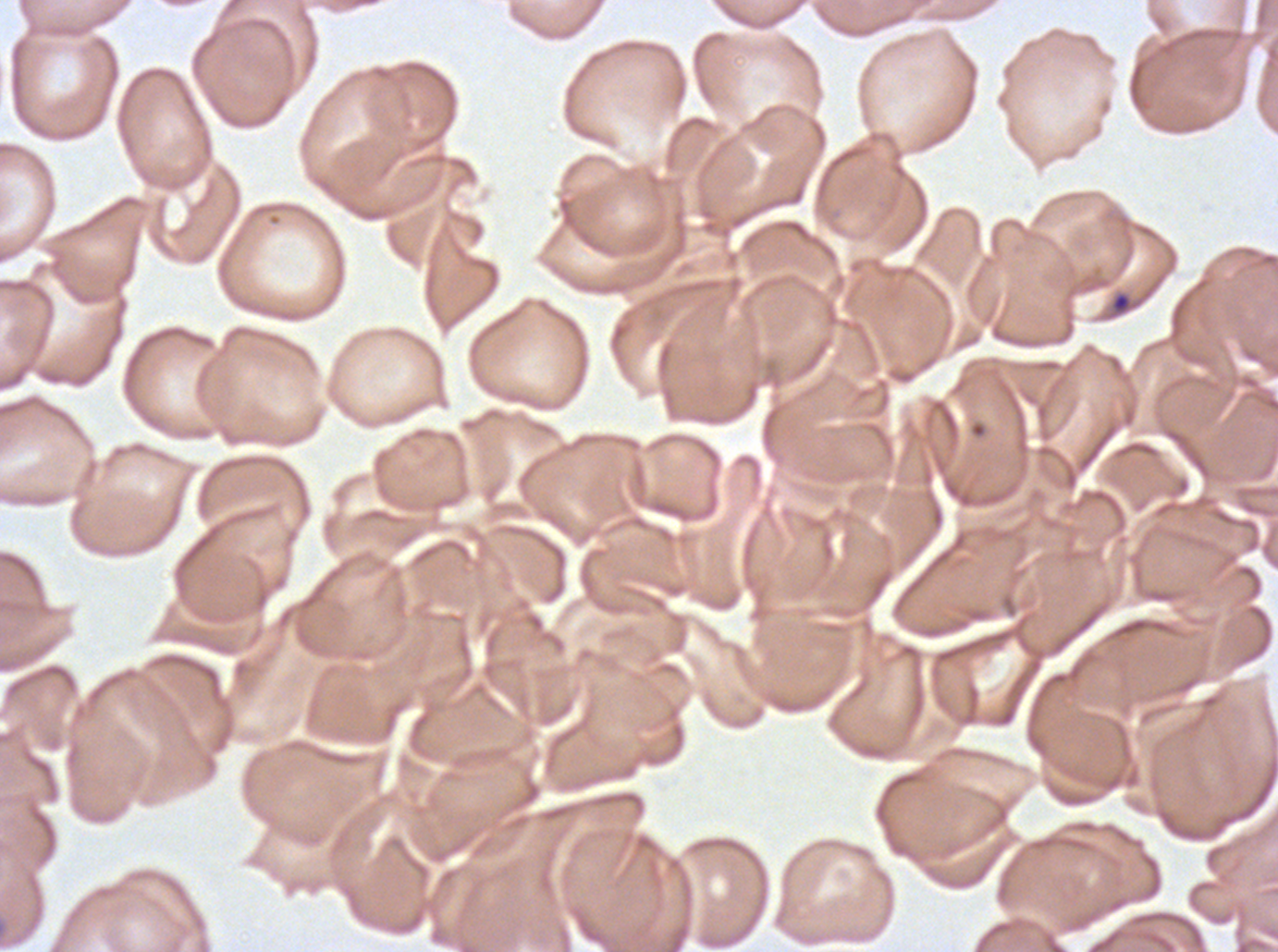
Approximate bounding boxes as (x1, y1, x2, y2) in pixels.
Summary:
  - Ring locations: (1112, 293, 1130, 312)
  - Specimen: Plasmodium falciparum cultured ex vivo for 24 to 48 hours, from a patient in The Gambia
  - Stain: Giemsa
  - Preparation: thin blood smear
  - Image size: 1278×952 pixels
  - Field of view: one sub-image of a larger composite